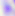
Toxoplasma gondii is seen. Captured at 400x magnification. Photomicrograph.